Report the malaria status of this cell.
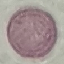

It is uninfected.

{
  "capture": "smartphone camera at the microscope eyepiece",
  "preparation": "thin smear",
  "stain": "Giemsa",
  "image_type": "cell patch, automatically extracted from a larger field of view and resized to 64 × 64 pixels"
}